Describe the morphology of the erythrocytes.
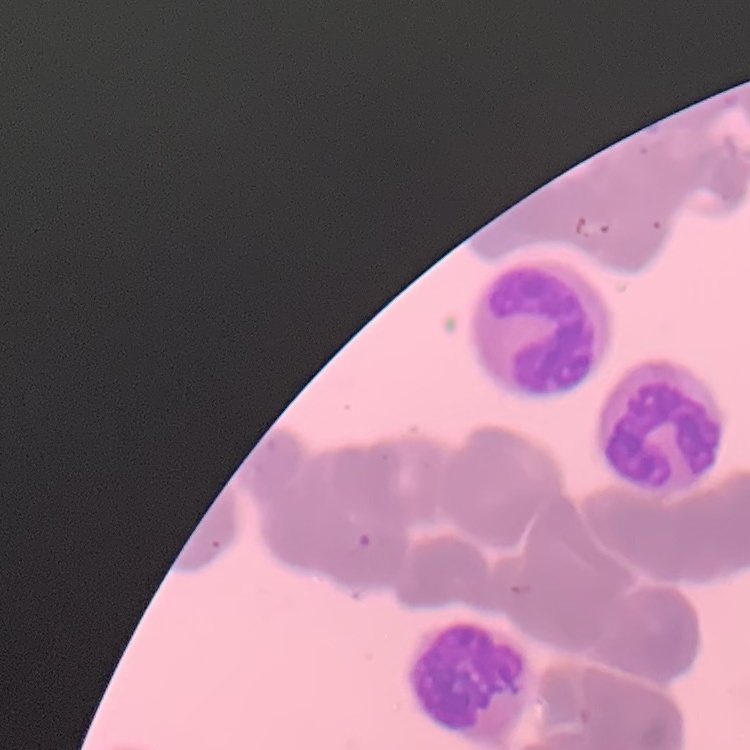
Rouleaux formation.

One tile cut from a larger photomicrograph. Thin blood smear. Stained with either Field's or Giemsa.